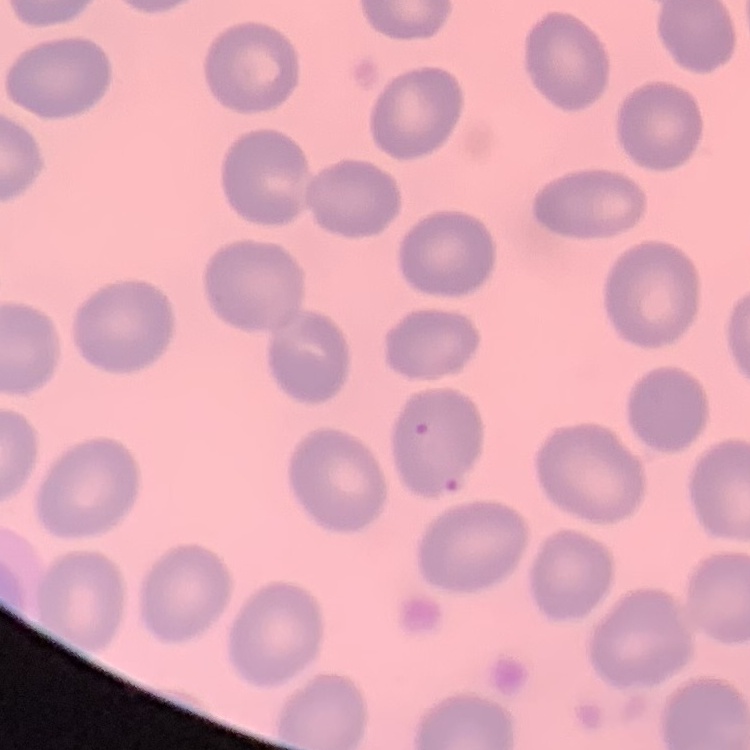
red blood cell morphology = no rouleaux formation
preparation = thin peripheral smear
image type = square crop of a larger photomicrograph
stain = Field's or Giemsa